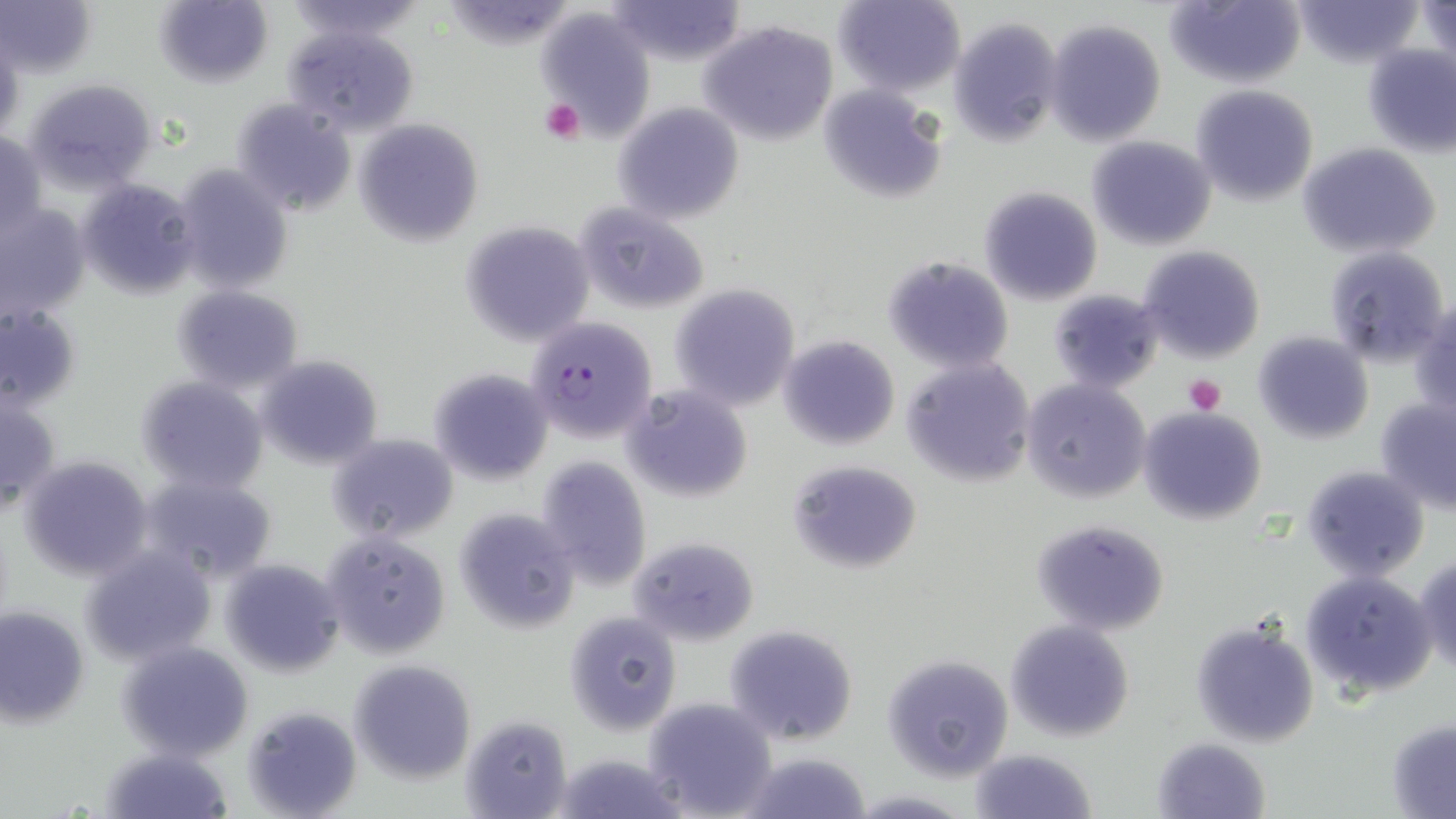
Approximate bounding boxes as named x1/y1/x2/y2 corners in pixels. Plasmodium falciparum-infected red blood cell locations: (x1=527, y1=316, x2=657, y2=443). Uninfected red blood cell locations: (x1=0, y1=0, x2=97, y2=78), (x1=154, y1=0, x2=274, y2=88), (x1=604, y1=0, x2=747, y2=68), (x1=834, y1=0, x2=965, y2=97), (x1=1164, y1=0, x2=1305, y2=89), (x1=1293, y1=0, x2=1421, y2=68), (x1=1418, y1=0, x2=1455, y2=73), (x1=538, y1=9, x2=655, y2=136), (x1=948, y1=16, x2=1063, y2=146), (x1=1045, y1=18, x2=1166, y2=146), (x1=699, y1=19, x2=840, y2=145), (x1=285, y1=26, x2=420, y2=135), (x1=1361, y1=42, x2=1456, y2=156), (x1=25, y1=77, x2=157, y2=192), (x1=817, y1=84, x2=948, y2=203), (x1=1190, y1=84, x2=1318, y2=206), (x1=232, y1=98, x2=358, y2=216), (x1=615, y1=102, x2=743, y2=226), (x1=354, y1=118, x2=484, y2=246), (x1=0, y1=129, x2=46, y2=242), (x1=1086, y1=135, x2=1217, y2=250), (x1=1298, y1=143, x2=1441, y2=258), (x1=173, y1=164, x2=295, y2=295), (x1=77, y1=178, x2=200, y2=300), (x1=978, y1=187, x2=1103, y2=306), (x1=574, y1=202, x2=711, y2=314), (x1=0, y1=205, x2=90, y2=318), (x1=462, y1=220, x2=595, y2=346), (x1=1137, y1=245, x2=1266, y2=365), (x1=1325, y1=247, x2=1451, y2=368), (x1=883, y1=256, x2=1015, y2=373), (x1=669, y1=284, x2=801, y2=411), (x1=172, y1=286, x2=303, y2=393), (x1=1048, y1=289, x2=1164, y2=393), (x1=1412, y1=300, x2=1456, y2=419), (x1=0, y1=303, x2=80, y2=412), (x1=1252, y1=331, x2=1375, y2=444), (x1=779, y1=335, x2=901, y2=450), (x1=255, y1=355, x2=384, y2=470), (x1=902, y1=359, x2=1036, y2=489), (x1=430, y1=367, x2=552, y2=485), (x1=137, y1=377, x2=268, y2=493), (x1=1019, y1=378, x2=1152, y2=504), (x1=620, y1=384, x2=754, y2=505), (x1=0, y1=396, x2=59, y2=512), (x1=1375, y1=396, x2=1456, y2=514), (x1=1137, y1=407, x2=1266, y2=525), (x1=325, y1=433, x2=458, y2=543), (x1=17, y1=453, x2=155, y2=581), (x1=536, y1=456, x2=652, y2=591), (x1=787, y1=460, x2=922, y2=573), (x1=1301, y1=465, x2=1429, y2=582), (x1=140, y1=473, x2=279, y2=583), (x1=454, y1=509, x2=579, y2=634), (x1=1031, y1=518, x2=1170, y2=636), (x1=324, y1=531, x2=453, y2=659), (x1=631, y1=537, x2=758, y2=646), (x1=80, y1=544, x2=217, y2=665), (x1=1414, y1=553, x2=1456, y2=678), (x1=219, y1=558, x2=344, y2=676), (x1=1299, y1=569, x2=1438, y2=700), (x1=0, y1=604, x2=89, y2=727), (x1=565, y1=612, x2=682, y2=735), (x1=1192, y1=617, x2=1320, y2=748), (x1=1004, y1=619, x2=1134, y2=742), (x1=723, y1=624, x2=860, y2=747), (x1=116, y1=640, x2=256, y2=762), (x1=883, y1=655, x2=1014, y2=780), (x1=349, y1=658, x2=478, y2=783), (x1=643, y1=697, x2=777, y2=818), (x1=243, y1=703, x2=362, y2=818), (x1=461, y1=713, x2=572, y2=818), (x1=1386, y1=718, x2=1456, y2=818), (x1=1151, y1=736, x2=1272, y2=819), (x1=101, y1=745, x2=235, y2=818), (x1=969, y1=747, x2=1096, y2=819), (x1=735, y1=749, x2=873, y2=819), (x1=553, y1=752, x2=687, y2=819). Platelet locations: (x1=538, y1=97, x2=586, y2=144), (x1=1184, y1=374, x2=1227, y2=415). Slide-level diagnosis: Plasmodium falciparum. May-Grünwald-Giemsa stain. Optical microscopy. 1000x magnification. Image is 1456×819 pixels. One field of a larger specimen. Thin blood film.